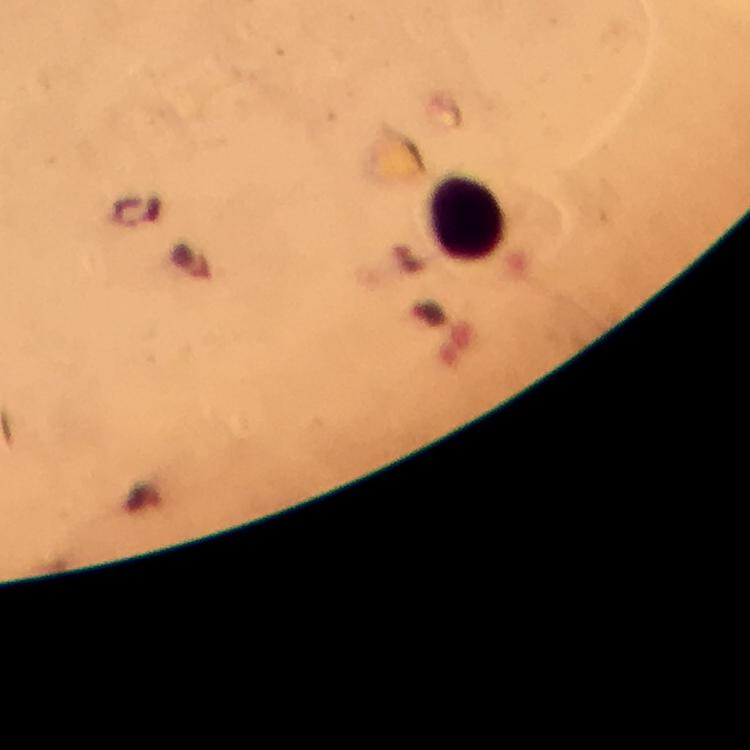

Approximate object centers, in pixels from the top-left corner.
Summary:
  - Leukocyte locations: (x=467, y=218)
  - Cropped from: a single field of view
  - Context: from a diagnostic examination for malaria
  - Preparation: thick smear
  - Capture: smartphone photograph through a microscope
  - Immersion oil: applied
  - Plasmodium parasites: none seen
  - Magnification: 100x
  - Stain: Giemsa
  - Image size: 750×750 pixels